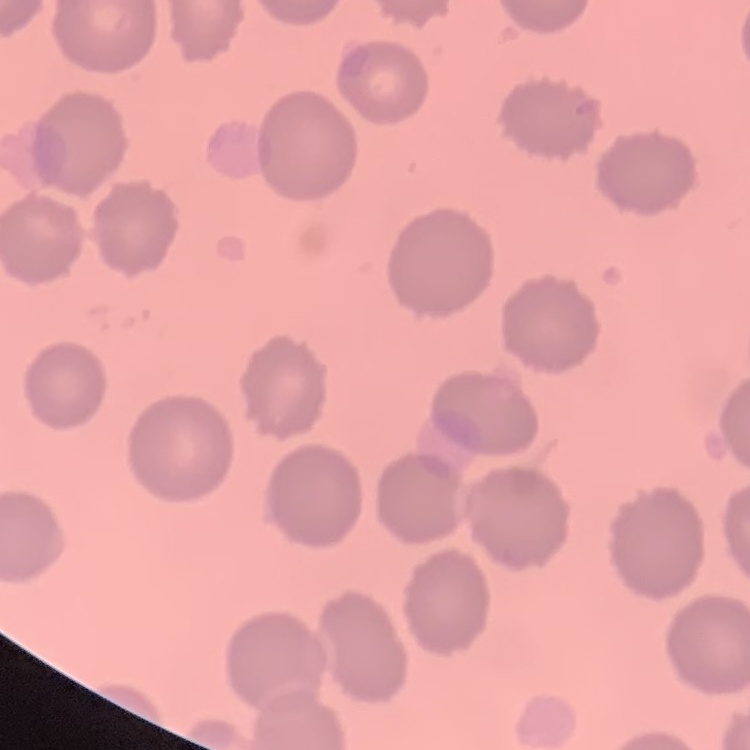
Summary:
  - Red blood cell morphology: no rouleaux formation
  - Preparation: thin blood smear
  - Image type: square crop of a larger photomicrograph
  - Stain: Field's or Giemsa